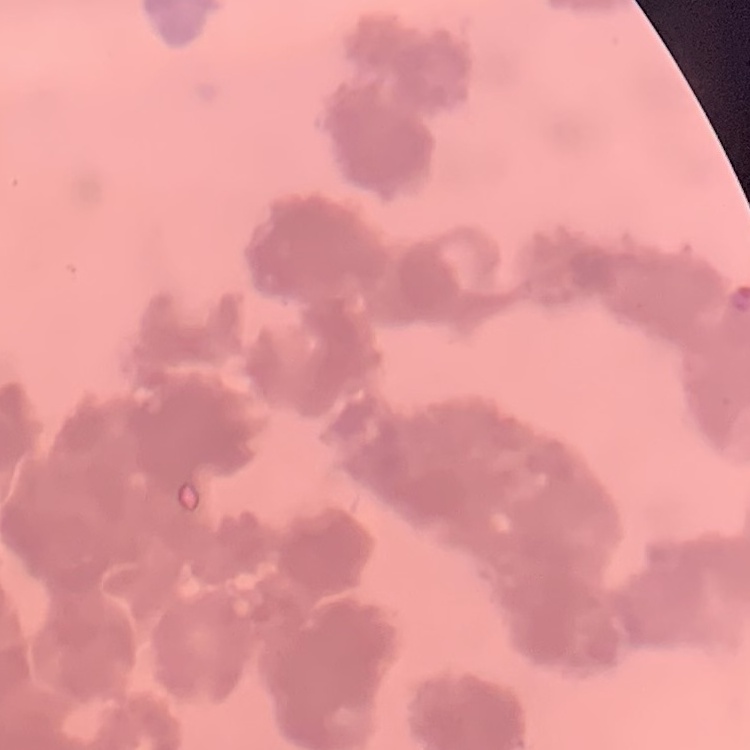
Summary:
  - Erythrocyte morphology: rouleaux formation
  - Stain: Field's or Giemsa
  - Image type: one tile cut from a larger photomicrograph
  - Preparation: thin peripheral smear